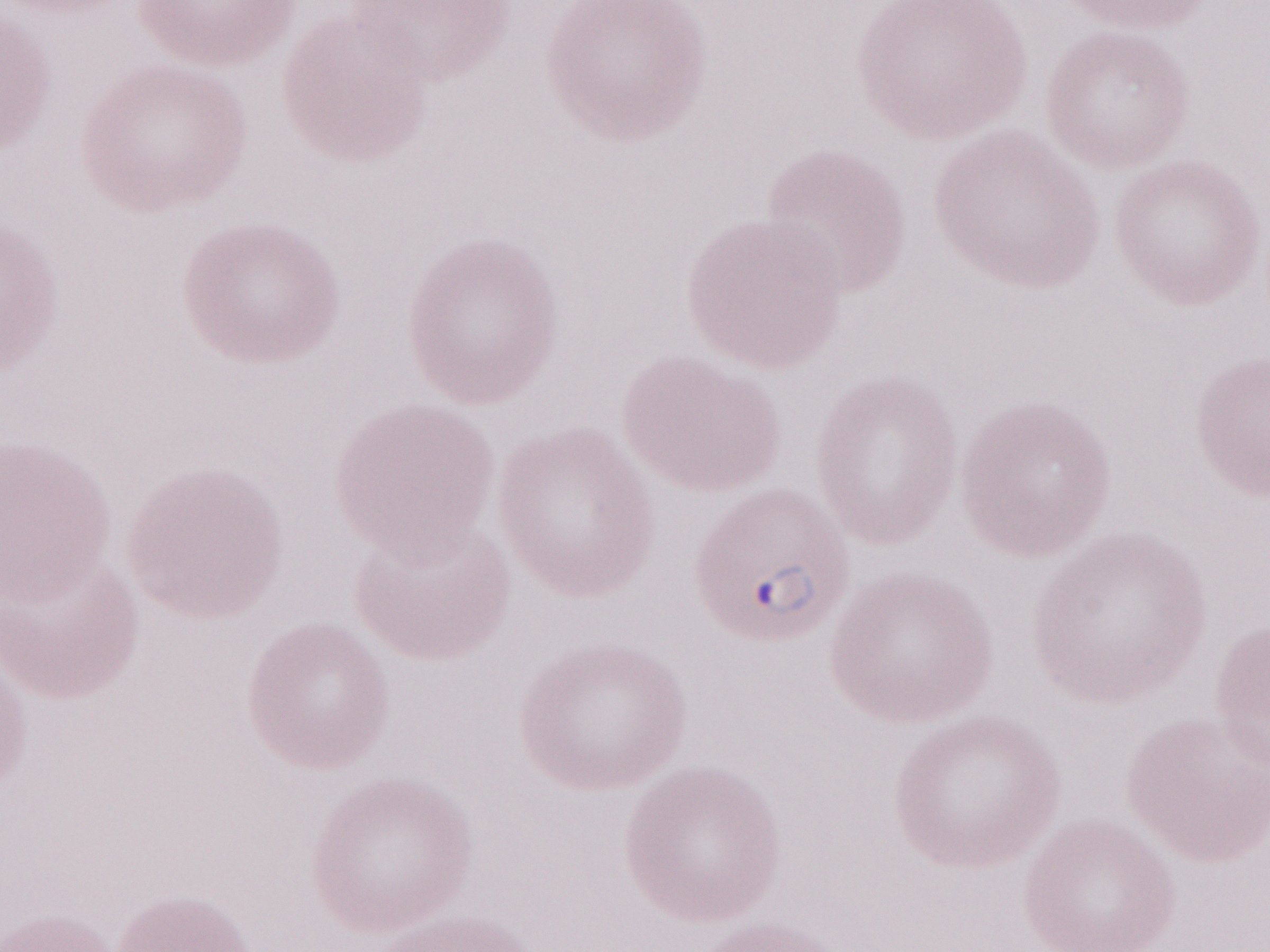

Image is 1270×952 pixels. Thin blood smear. Olympus BX43 microscope and DP73 digital camera. May-Grünwald-Giemsa stain. 1,000x magnification. One field of this slide. Malaria diagnosis (patient-level): positive.